Assess this cell for malaria.
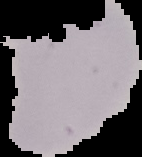
Uninfected.

Summary:
  - Preparation: thin blood smear
  - Image size: 142×157 pixels
  - Image type: segmented cell region on a black background